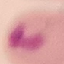
{
  "malaria_status": "uninfected",
  "preparation": "thin smear",
  "capture": "smartphone through the microscope eyepiece",
  "stain": "Giemsa",
  "image_type": "automatically extracted cell patch, resized to 64 × 64 pixels"
}